Classify this cell by malaria status.
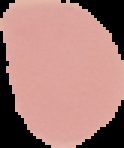
It is uninfected.

Summary:
  - Preparation: thin blood film
  - Image type: segmented cell region on a black background
  - Image size: 124×148 pixels